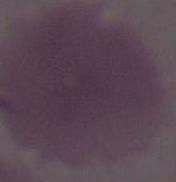
A red blood cell is seen. Photomicrograph. Captured at 1000x magnification.